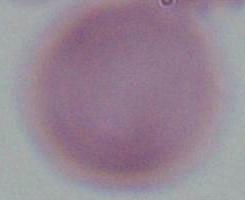
{
  "magnification": "1000x",
  "modality": "photomicrograph",
  "identification": "erythrocyte"
}